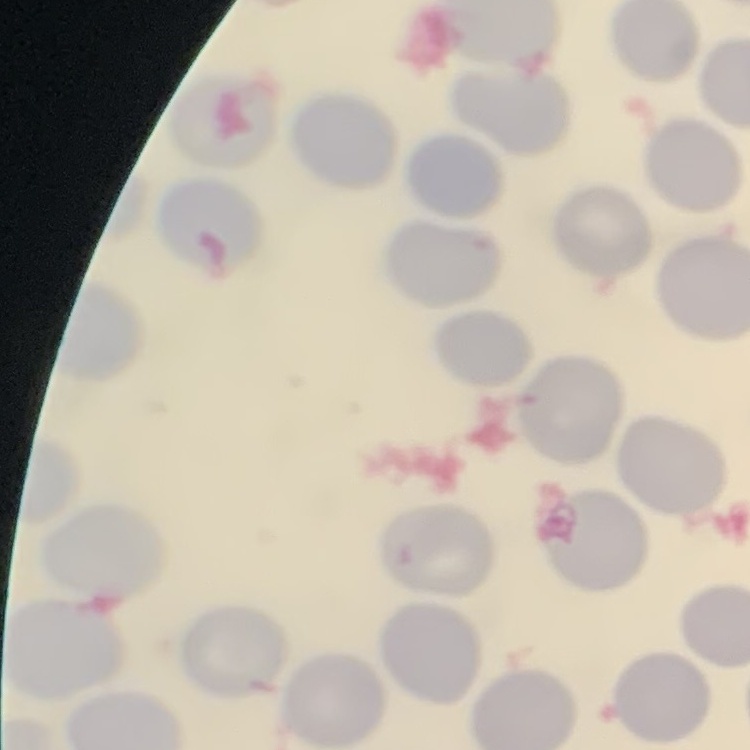

The red blood cells show no rouleaux formation. Field's or Giemsa stain. Thin blood film. Square crop of a larger photomicrograph.